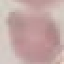

result: no malaria parasites seen
capture: smartphone camera at the microscope eyepiece
stain: Giemsa
preparation: thin smear
image_type: cell patch, automatically extracted from a larger field of view and resized to 64 × 64 pixels